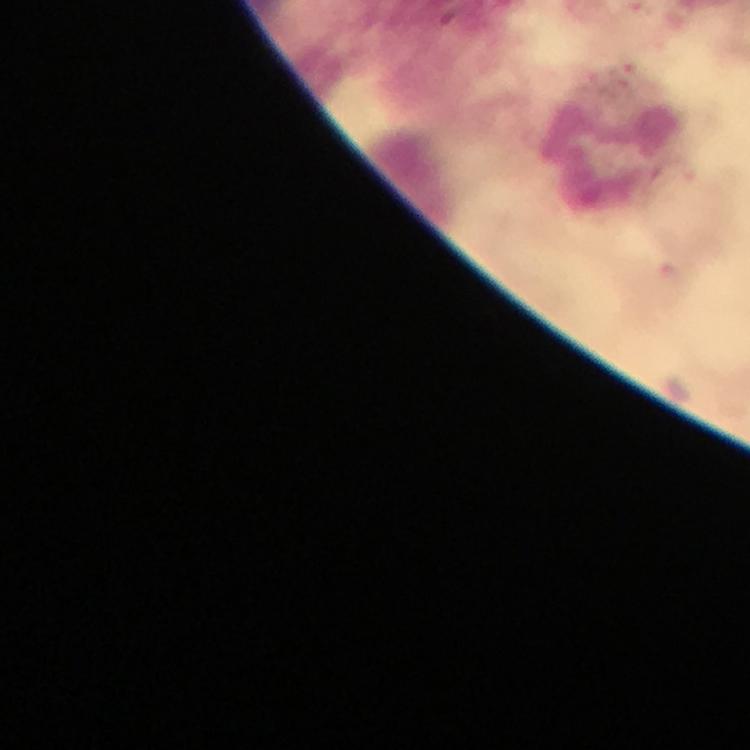
Approximate centers as {x, y} in pixels.
Summary:
  - Malaria parasite locations: {623, 73}
  - Leukocyte locations: {615, 156}
  - Stain: Giemsa
  - Image size: 750×750 pixels
  - Context: from a diagnostic examination for malaria
  - Capture: smartphone photograph through a microscope
  - Cropped from: one field of view
  - Immersion oil: used
  - Magnification: 100x
  - Preparation: thick blood film